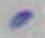 1000x magnification. Toxoplasma gondii is shown. Photomicrograph.